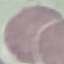
malaria status = uninfected
image type = automatically extracted cell patch, resized to 64 × 64 pixels
capture = smartphone camera at the microscope eyepiece
preparation = thin blood smear
stain = Giemsa